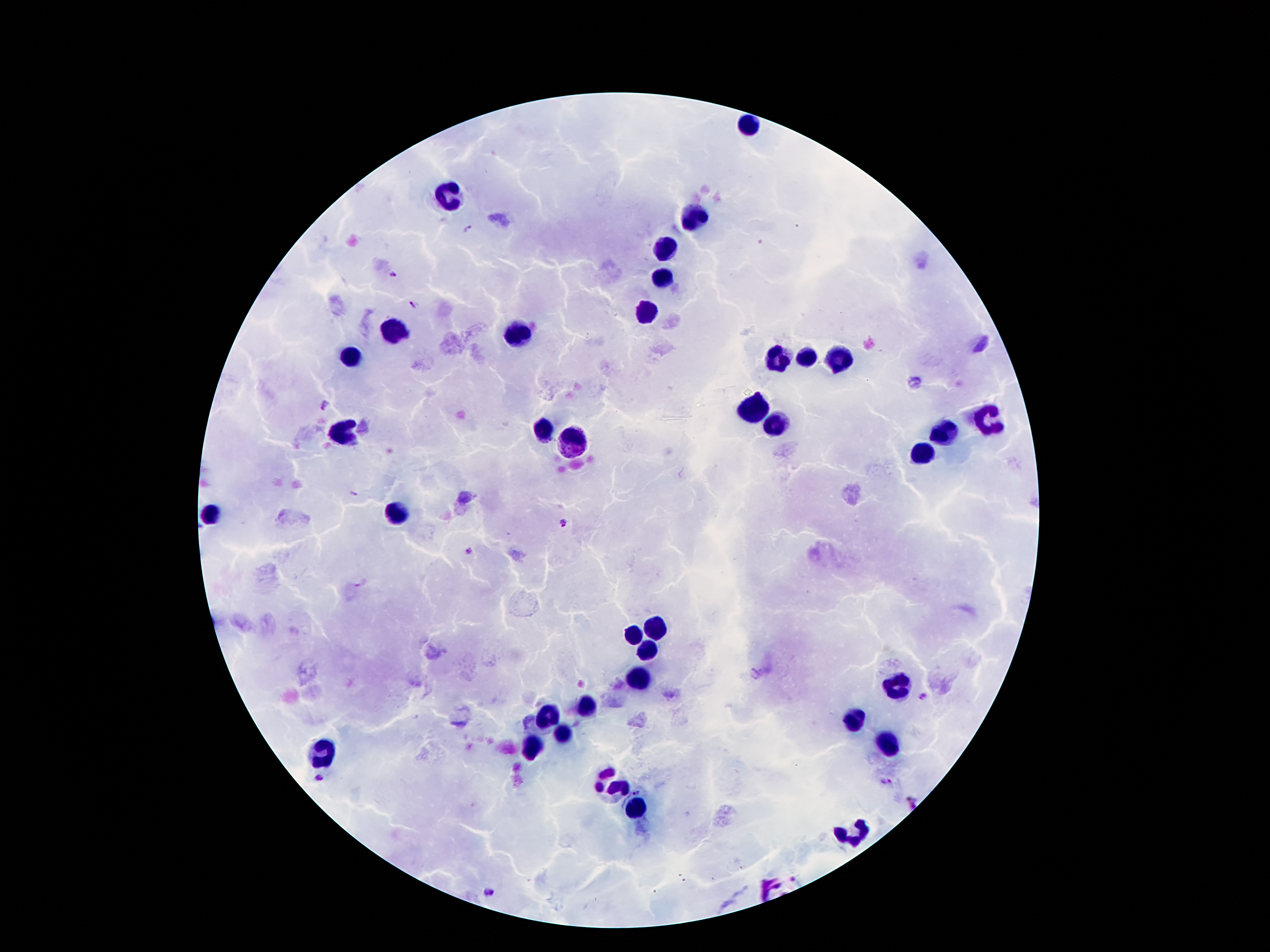

Approximate centers as {x, y} in pixels.
Summary:
  - Leukocyte locations: {750, 124}, {447, 197}, {695, 218}, {666, 248}, {662, 281}, {645, 311}, {393, 328}, {515, 332}, {353, 355}, {806, 357}, {777, 359}, {838, 359}, {748, 410}, {987, 420}, {775, 422}, {344, 429}, {544, 429}, {945, 433}, {573, 443}, {922, 456}, {212, 513}, {397, 515}, {657, 628}, {634, 632}, {647, 653}, {640, 674}, {897, 685}, {588, 706}, {548, 717}, {855, 719}, {563, 733}, {533, 746}, {890, 746}, {325, 750}, {607, 780}, {632, 809}, {852, 838}
  - Plasmodium parasite locations: {468, 229}, {394, 275}, {412, 303}, {325, 404}, {355, 493}, {562, 522}, {470, 551}, {363, 583}, {924, 696}, {321, 778}, {885, 782}, {636, 790}, {910, 804}, {489, 891}
  - Capture: smartphone through the microscope eyepiece
  - Field of view: one from this slide
  - Magnification: 100x
  - Stain: Giemsa
  - Preparation: thick peripheral-blood smear
  - Image size: 1270×952 pixels
  - Patient malaria status: infected with Plasmodium falciparum